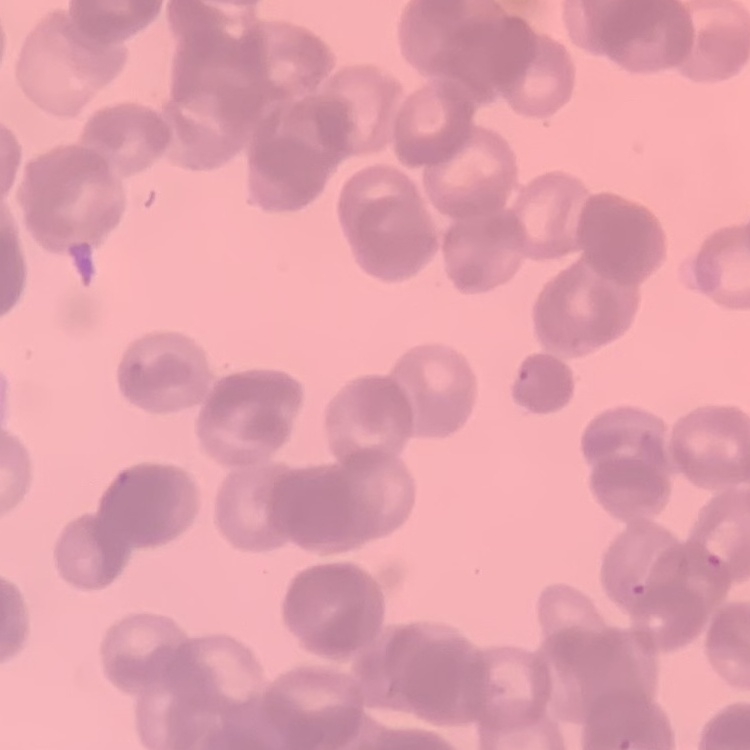

erythrocyte_morphology: rouleaux formation
image_type: square crop of a larger photomicrograph
stain: Field's or Giemsa
preparation: thin blood film